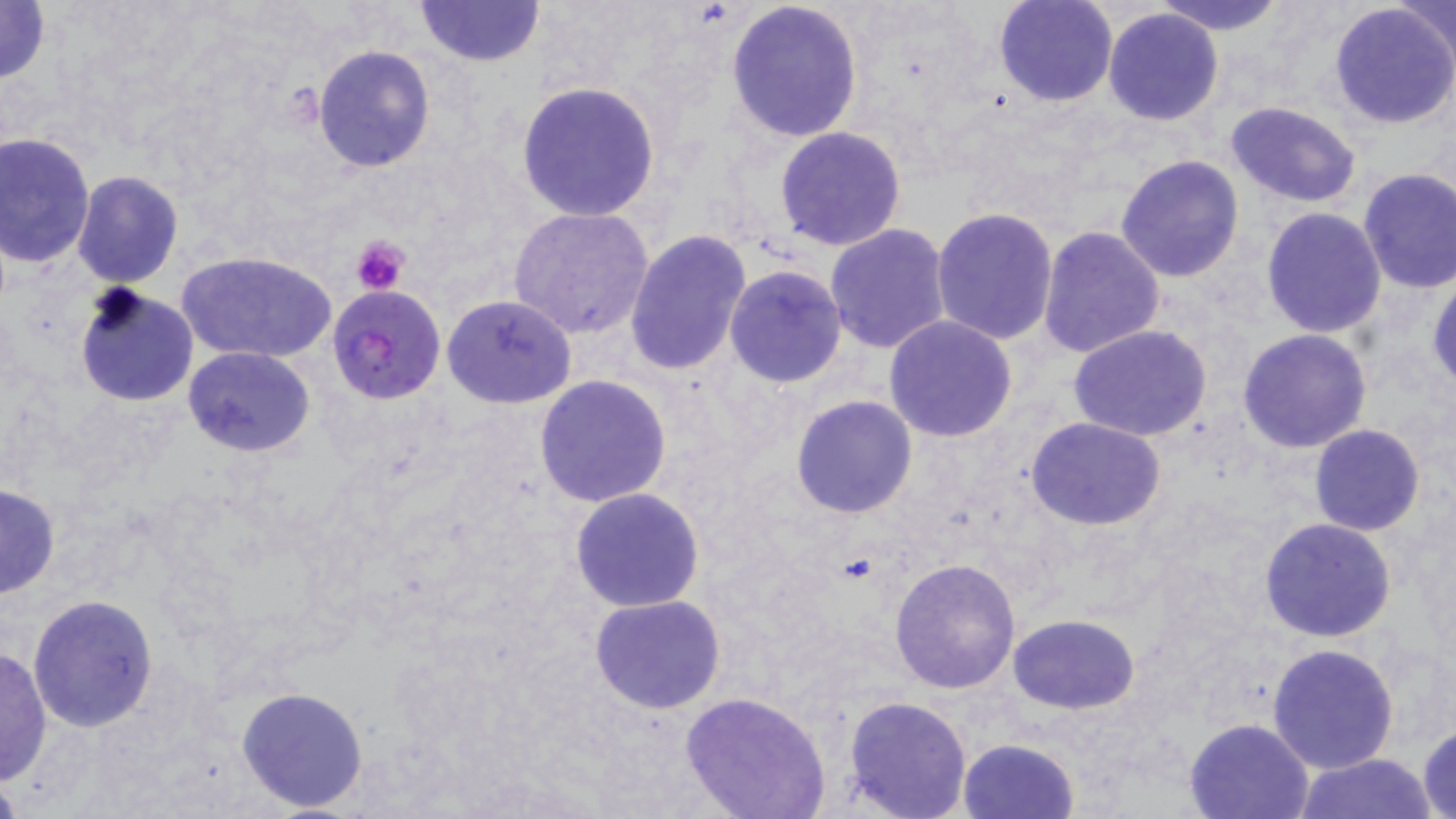
Summary:
  - Coordinate format: approximate bounding boxes as (x1,y1)-(x2,y2) corner pairs in pixels
  - Uninfected red blood cell locations: (0,0)-(50,86), (414,0)-(546,69), (724,0)-(863,143), (993,0)-(1117,107), (1155,0)-(1288,35), (1395,2)-(1456,68), (1329,4)-(1456,131), (1102,7)-(1224,126), (312,45)-(436,172), (513,79)-(662,222), (1224,101)-(1362,207), (773,126)-(906,251), (0,129)-(97,270), (1115,154)-(1245,283), (1356,169)-(1456,295), (71,170)-(184,288), (509,205)-(656,342), (1260,206)-(1387,339), (931,207)-(1059,344), (824,224)-(953,355), (1038,224)-(1166,360), (623,229)-(754,376), (175,250)-(338,363), (725,264)-(849,386), (1428,274)-(1456,389), (74,284)-(198,407), (441,293)-(578,409), (883,315)-(1019,442), (1069,326)-(1211,442), (1238,328)-(1372,452), (182,347)-(314,458), (534,374)-(672,507), (791,394)-(919,518), (1025,417)-(1168,531), (1308,425)-(1426,536), (1,483)-(61,600), (571,487)-(705,611), (1260,518)-(1396,643), (890,555)-(1021,694), (26,594)-(159,731), (589,595)-(727,714), (1007,614)-(1139,714), (1268,642)-(1400,775), (0,645)-(52,784), (236,685)-(370,814), (679,692)-(830,819), (841,695)-(973,819), (1183,717)-(1316,818), (1417,724)-(1456,817), (957,738)-(1081,819), (1297,752)-(1439,818)
  - Plasmodium falciparum-infected red blood cell locations: (327,285)-(448,406)
  - Platelet locations: (353,235)-(408,296)
  - Slide-level diagnosis: Plasmodium falciparum
  - Field of view: one of a larger specimen
  - Preparation: thin blood film
  - Modality: light microscopy
  - Magnification: 1000x
  - Stain: May-Grünwald-Giemsa
  - Image size: 1456×819 pixels